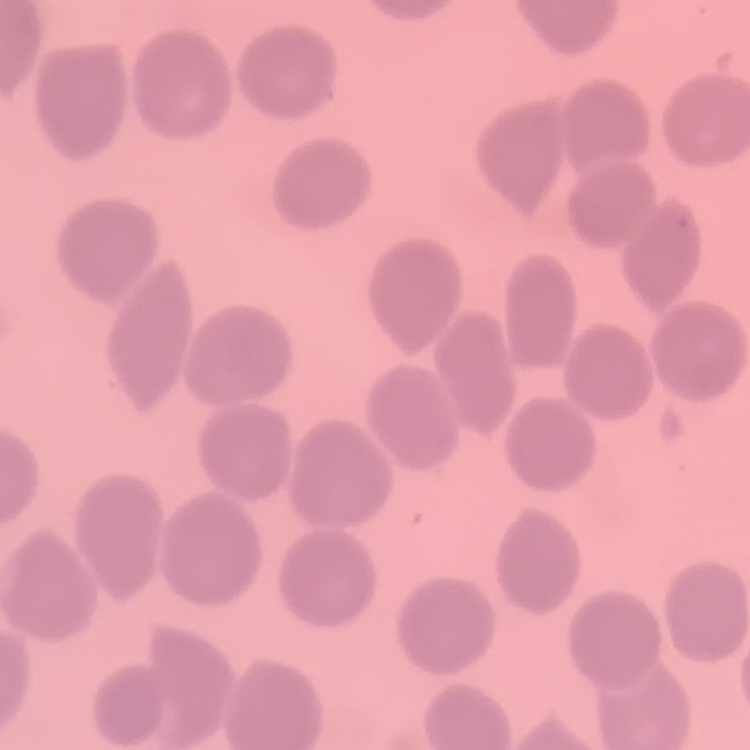
red blood cell morphology = no rouleaux formation
image type = one tile cut from a larger photomicrograph
preparation = thin blood smear
stain = Field's or Giemsa